Name the parasite shown.
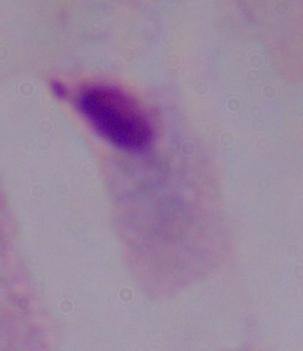

This is a trichomonad.

Micrograph. Captured at 1000x magnification.